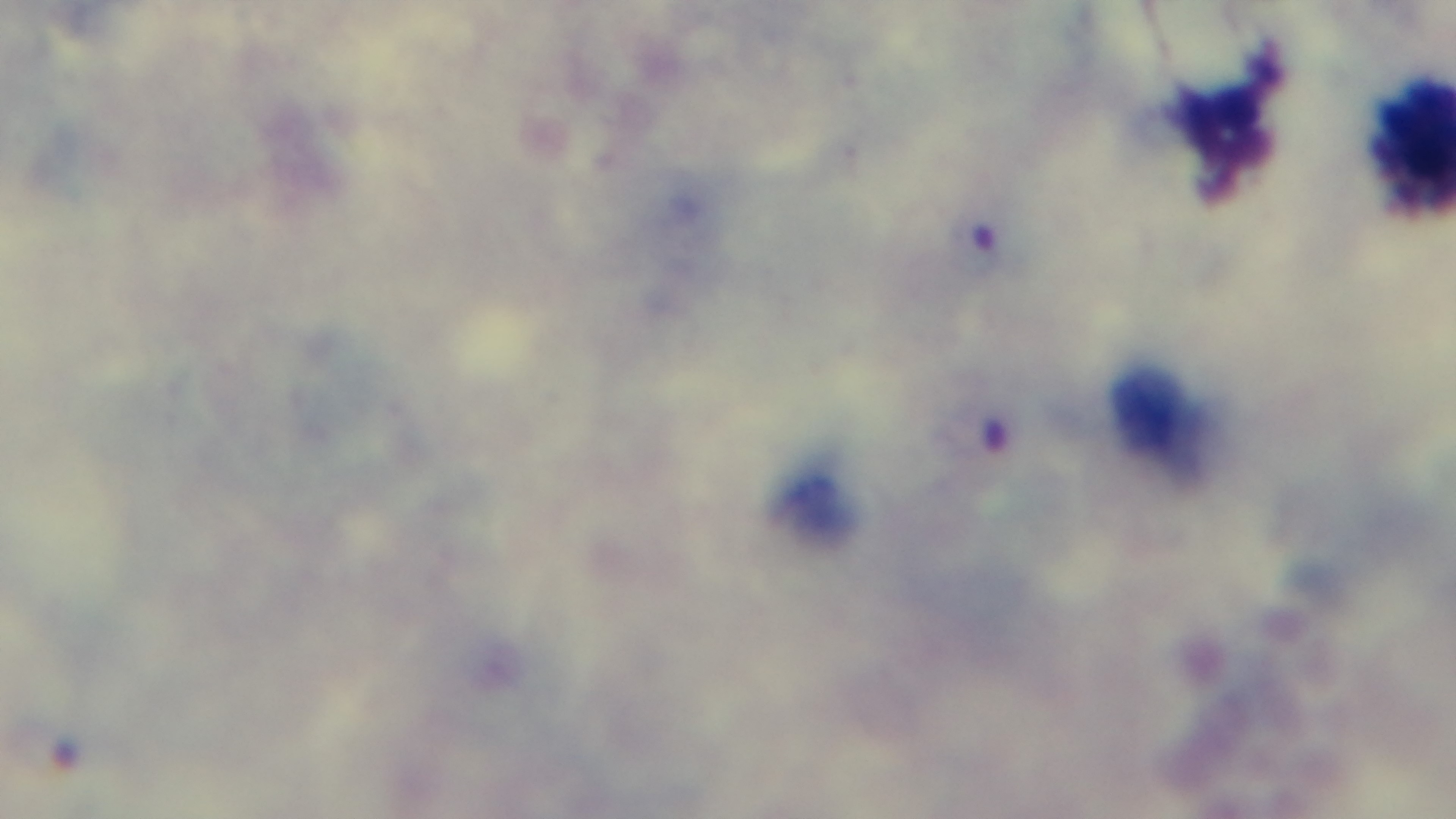
Preparation: thick. One field from the slide. Light microscopy. Giemsa stain. Malaria status: positive. Oil-immersion objective, 100x. Mounted 4K digital camera.